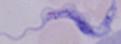

Photomicrograph. 1000x magnification. A trypanosome is shown.